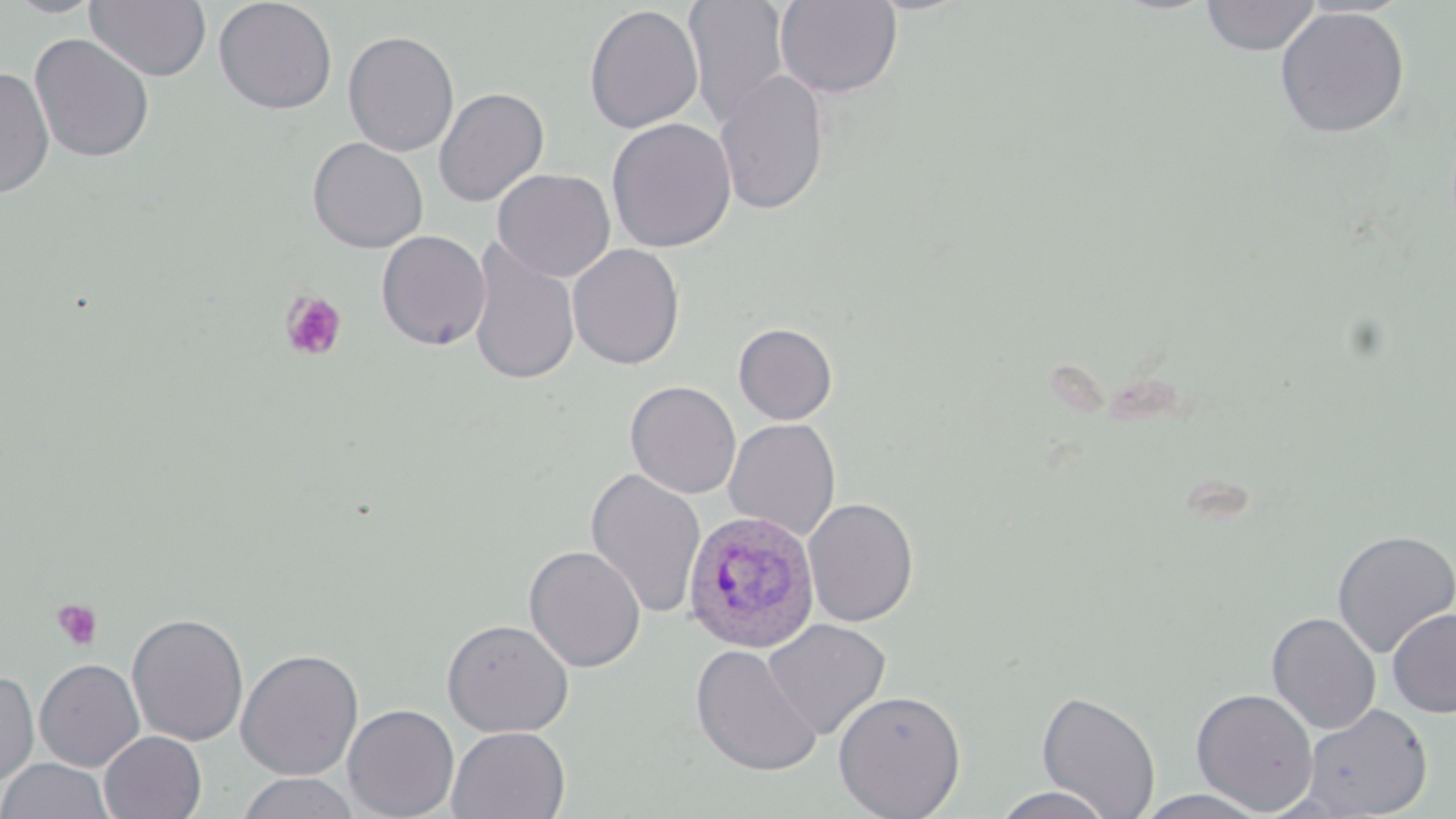
Summary:
  - Coordinate format: approximate bounding boxes as (x1, y1, x2, y2) in pixels
  - Plasmodium ovale-infected red blood cell locations: (682, 510, 820, 654)
  - Platelet locations: (280, 291, 347, 361), (50, 598, 104, 651)
  - Uninfected red blood cell locations: (84, 0, 212, 82), (213, 0, 338, 115), (683, 0, 791, 127), (774, 0, 903, 99), (1200, 0, 1321, 56), (583, 4, 703, 134), (1274, 6, 1410, 139), (342, 30, 460, 157), (29, 33, 155, 163), (0, 67, 55, 200), (713, 70, 831, 216), (433, 87, 549, 207), (606, 118, 737, 253), (307, 137, 428, 253), (492, 168, 615, 282), (375, 230, 491, 351), (467, 240, 579, 387), (567, 243, 685, 369), (733, 322, 838, 425), (625, 381, 742, 499), (723, 418, 841, 541), (585, 467, 707, 620), (803, 497, 919, 627), (1332, 529, 1456, 657), (524, 545, 646, 672), (1387, 608, 1456, 717), (126, 612, 249, 747), (1266, 612, 1381, 734), (441, 619, 574, 737), (762, 619, 891, 741), (690, 644, 822, 777), (236, 648, 363, 781), (34, 659, 145, 771), (0, 671, 40, 786), (1191, 688, 1318, 815), (833, 689, 966, 819), (1036, 689, 1161, 819), (342, 703, 460, 819), (1301, 703, 1433, 817), (446, 726, 571, 818), (99, 731, 206, 819), (0, 758, 114, 819), (235, 772, 359, 818), (990, 786, 1116, 819), (1132, 789, 1272, 818)
  - Slide-level diagnosis: Plasmodium ovale
  - Preparation: thin blood film
  - Field of view: one of a larger specimen
  - Image size: 1456×819 pixels
  - Modality: light microscopy
  - Magnification: 1000x
  - Stain: May-Grünwald-Giemsa